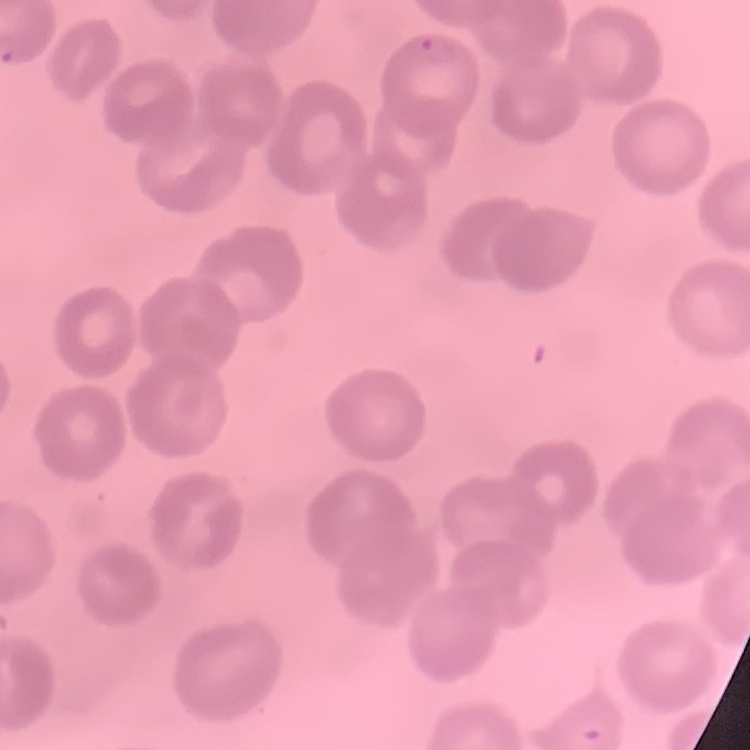

Summary:
  - Erythrocyte morphology: no rouleaux formation
  - Stain: Field's or Giemsa
  - Image type: square crop of a larger photomicrograph
  - Preparation: thin peripheral smear